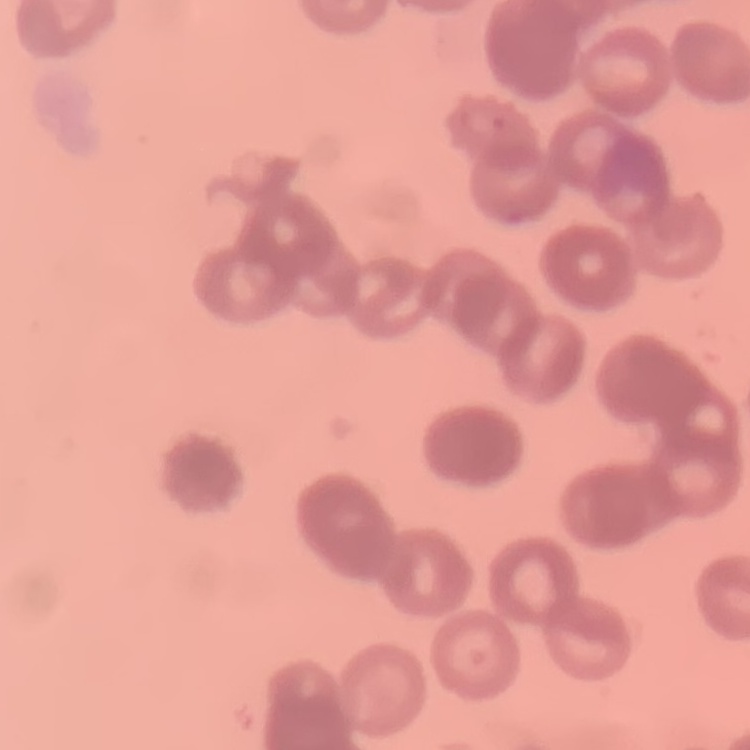
red_blood_cell_morphology: rouleaux formation
stain: Field's or Giemsa
preparation: thin peripheral smear
image_type: square crop of a larger photomicrograph